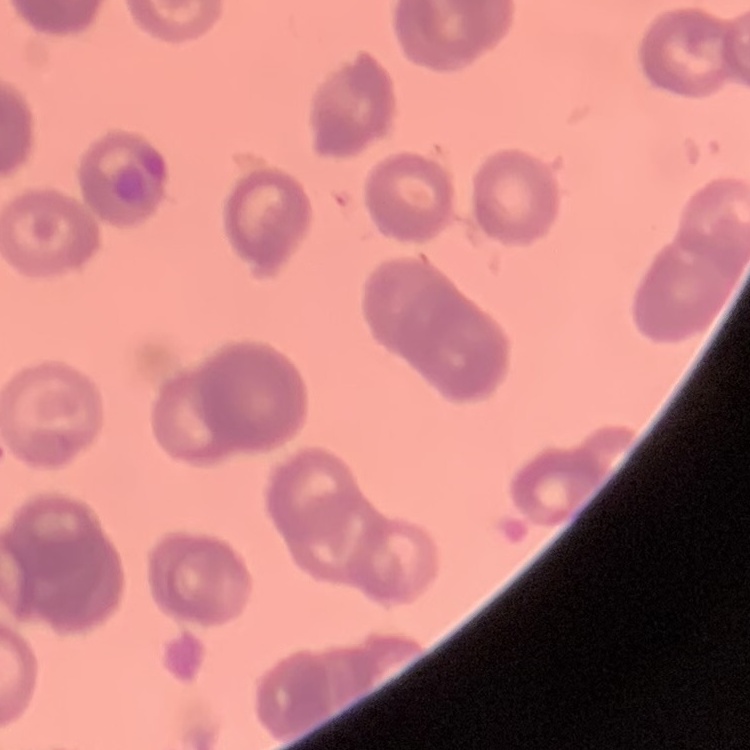

Summary:
  - Erythrocyte morphology: rouleaux formation
  - Preparation: thin blood film
  - Stain: Field's or Giemsa
  - Image type: one tile cut from a larger photomicrograph